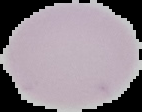

{
  "result": "no malaria parasites detected",
  "image_type": "segmented cell region on a black background",
  "preparation": "thin blood smear",
  "image_size": "142×112 pixels"
}